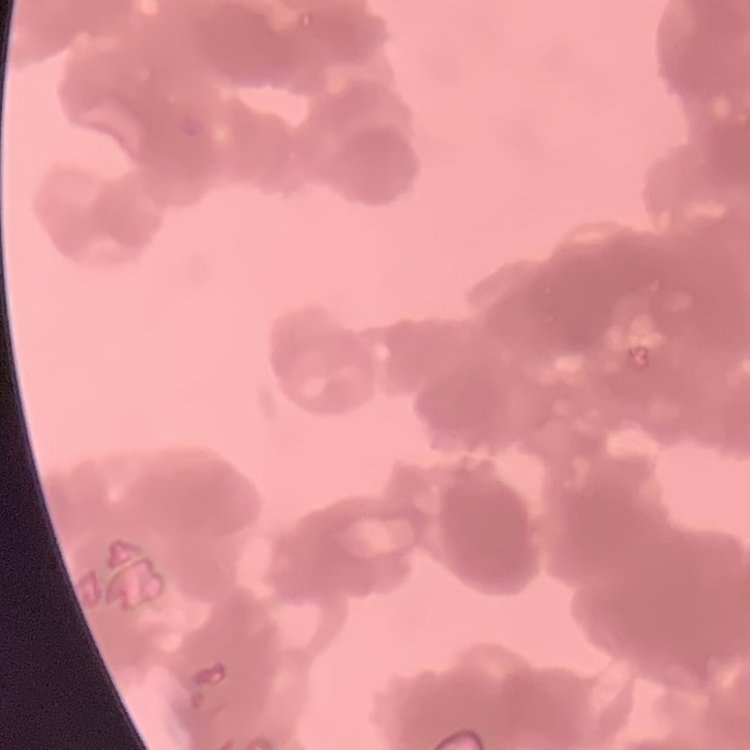

The erythrocytes exhibit rouleaux formation. Thin peripheral smear. Field's or Giemsa stain. Square crop of a larger photomicrograph.